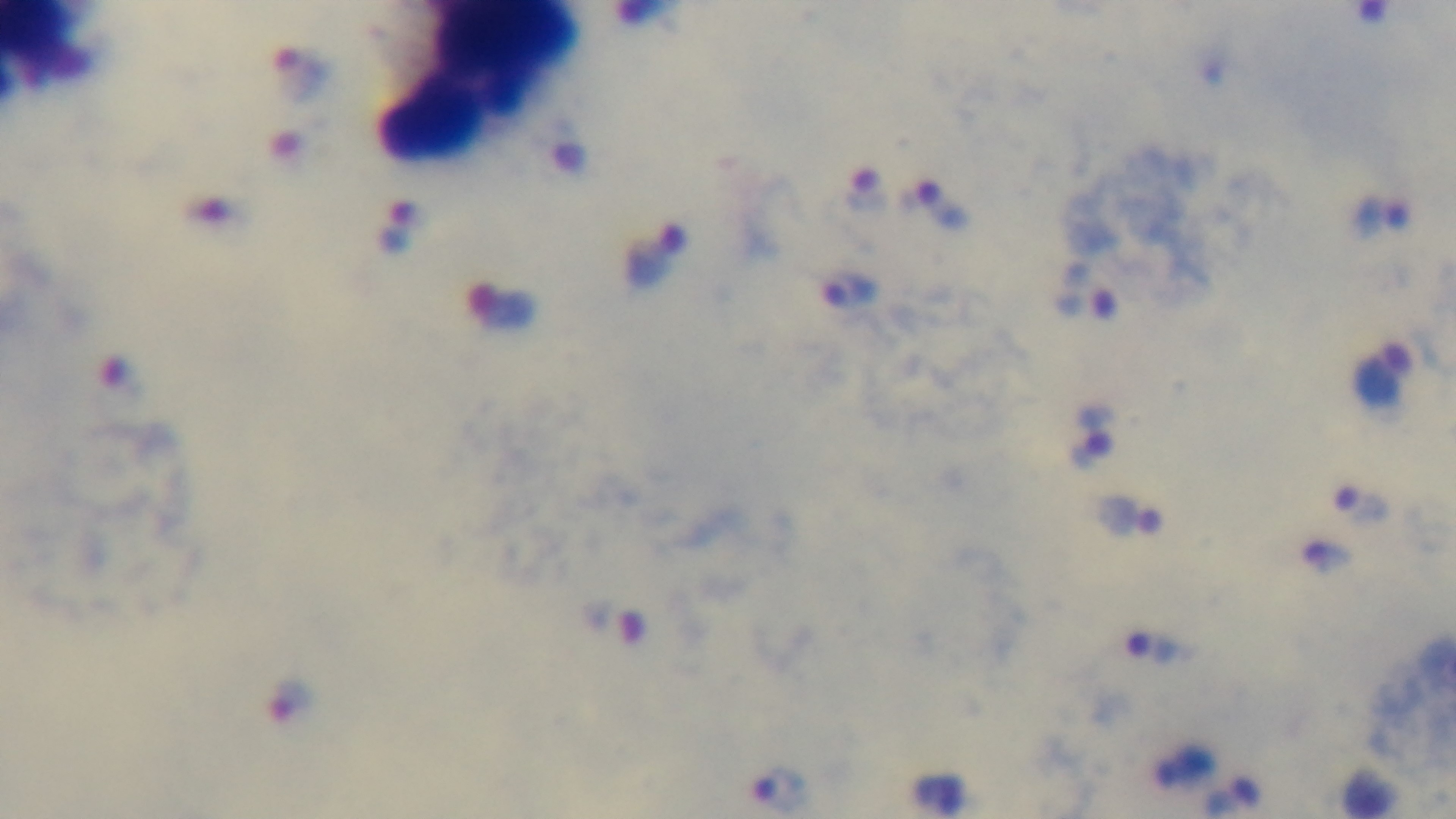
Giemsa stain. Malaria status: infected. Photomicrograph. One field from the slide. Captured with a mounted 4K digital camera. Preparation: thick blood film. 100x oil-immersion objective.